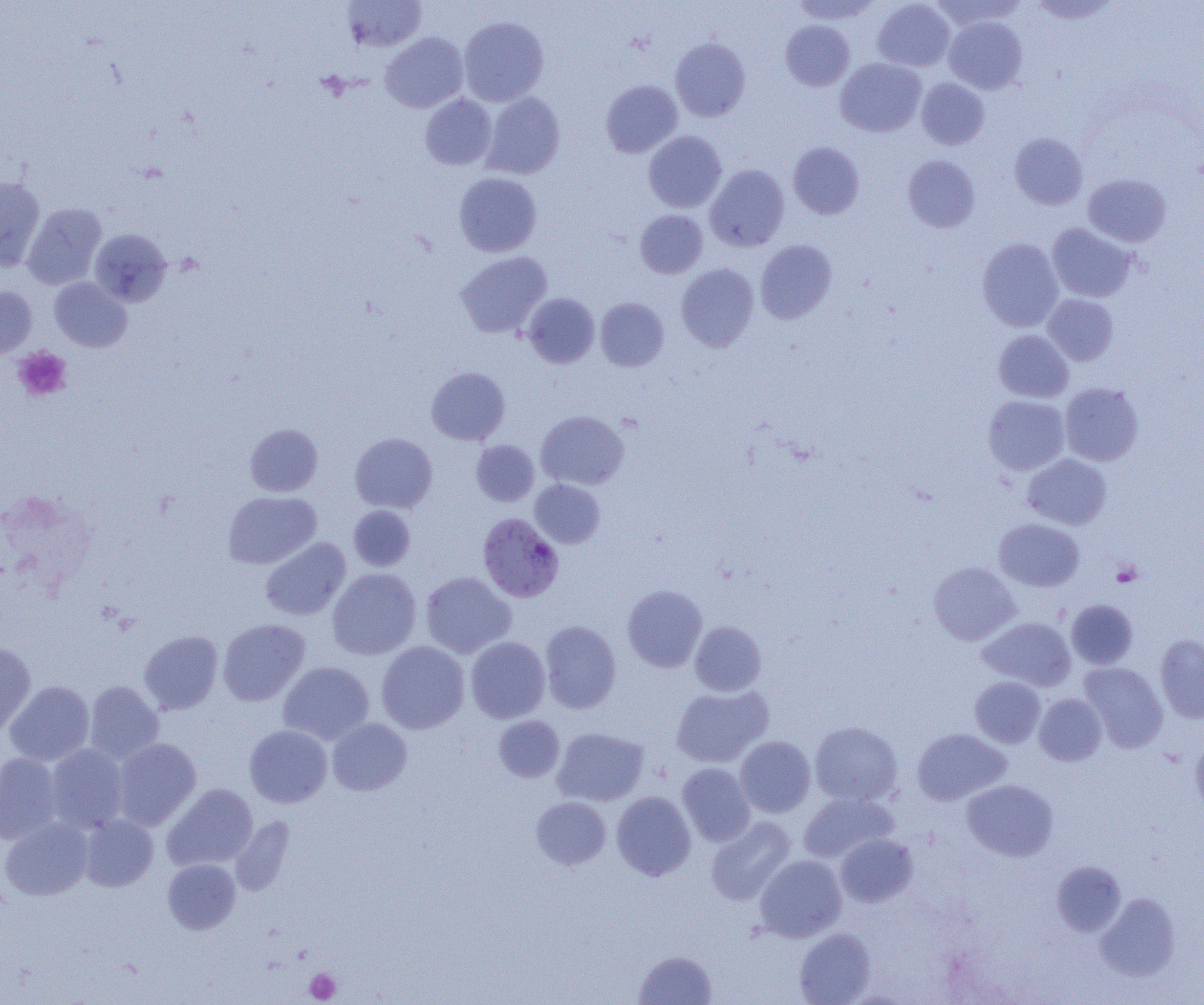
Summary:
  - Coordinate format: approximate bounding boxes as named x1/y1/x2/y2 corners in pixels
  - Platelet locations: (x1=14, y1=347, x2=72, y2=401), (x1=1111, y1=561, x2=1143, y2=587), (x1=305, y1=968, x2=341, y2=1003)
  - Uninfected red blood cell locations: (x1=791, y1=0, x2=881, y2=26), (x1=872, y1=0, x2=955, y2=72), (x1=928, y1=0, x2=1027, y2=31), (x1=341, y1=1, x2=427, y2=51), (x1=458, y1=16, x2=549, y2=107), (x1=943, y1=16, x2=1027, y2=94), (x1=780, y1=20, x2=855, y2=90), (x1=380, y1=32, x2=469, y2=112), (x1=670, y1=37, x2=750, y2=121), (x1=835, y1=58, x2=926, y2=137), (x1=916, y1=78, x2=989, y2=150), (x1=600, y1=80, x2=682, y2=158), (x1=481, y1=92, x2=565, y2=179), (x1=419, y1=94, x2=497, y2=170), (x1=643, y1=130, x2=726, y2=213), (x1=1009, y1=132, x2=1088, y2=210), (x1=788, y1=141, x2=865, y2=219), (x1=903, y1=155, x2=980, y2=232), (x1=705, y1=164, x2=789, y2=251), (x1=454, y1=172, x2=541, y2=257), (x1=1083, y1=174, x2=1171, y2=247), (x1=0, y1=176, x2=45, y2=270), (x1=22, y1=203, x2=106, y2=290), (x1=635, y1=210, x2=708, y2=279), (x1=1047, y1=223, x2=1137, y2=302), (x1=89, y1=229, x2=172, y2=307), (x1=977, y1=238, x2=1063, y2=332), (x1=755, y1=240, x2=837, y2=324), (x1=455, y1=251, x2=552, y2=338), (x1=676, y1=263, x2=759, y2=351), (x1=49, y1=277, x2=132, y2=352), (x1=0, y1=286, x2=37, y2=359), (x1=522, y1=293, x2=600, y2=368), (x1=1042, y1=294, x2=1118, y2=366), (x1=595, y1=297, x2=669, y2=371), (x1=993, y1=330, x2=1074, y2=403), (x1=427, y1=367, x2=510, y2=445), (x1=1060, y1=382, x2=1144, y2=466), (x1=983, y1=395, x2=1070, y2=475), (x1=535, y1=410, x2=629, y2=490), (x1=245, y1=423, x2=323, y2=497), (x1=350, y1=433, x2=438, y2=513), (x1=471, y1=440, x2=539, y2=506), (x1=1022, y1=454, x2=1112, y2=530), (x1=530, y1=479, x2=605, y2=548), (x1=223, y1=491, x2=321, y2=569), (x1=348, y1=505, x2=416, y2=571), (x1=994, y1=518, x2=1085, y2=591), (x1=260, y1=537, x2=351, y2=620), (x1=929, y1=562, x2=1021, y2=645), (x1=327, y1=568, x2=421, y2=660), (x1=420, y1=571, x2=516, y2=658), (x1=622, y1=584, x2=707, y2=672), (x1=1066, y1=599, x2=1138, y2=669), (x1=978, y1=616, x2=1076, y2=691), (x1=217, y1=619, x2=310, y2=706), (x1=540, y1=620, x2=621, y2=713), (x1=689, y1=621, x2=766, y2=695), (x1=139, y1=630, x2=223, y2=714), (x1=1155, y1=634, x2=1204, y2=723), (x1=466, y1=636, x2=550, y2=723), (x1=376, y1=641, x2=470, y2=734), (x1=0, y1=643, x2=36, y2=738), (x1=278, y1=661, x2=374, y2=745), (x1=1079, y1=662, x2=1168, y2=752), (x1=970, y1=676, x2=1046, y2=748), (x1=4, y1=680, x2=95, y2=766), (x1=84, y1=681, x2=163, y2=763), (x1=671, y1=685, x2=773, y2=768), (x1=1034, y1=694, x2=1107, y2=766), (x1=493, y1=715, x2=565, y2=783), (x1=328, y1=718, x2=412, y2=795), (x1=809, y1=721, x2=902, y2=806), (x1=244, y1=724, x2=332, y2=807), (x1=552, y1=727, x2=649, y2=806), (x1=912, y1=728, x2=1011, y2=805), (x1=735, y1=736, x2=816, y2=818), (x1=1190, y1=736, x2=1204, y2=817), (x1=112, y1=738, x2=201, y2=830), (x1=45, y1=744, x2=129, y2=833), (x1=0, y1=753, x2=62, y2=844), (x1=677, y1=762, x2=756, y2=846), (x1=962, y1=779, x2=1058, y2=861), (x1=163, y1=783, x2=258, y2=870), (x1=611, y1=791, x2=696, y2=880), (x1=798, y1=792, x2=898, y2=863), (x1=531, y1=797, x2=611, y2=870), (x1=78, y1=815, x2=158, y2=891), (x1=705, y1=816, x2=796, y2=905), (x1=0, y1=817, x2=94, y2=901), (x1=835, y1=833, x2=917, y2=907), (x1=755, y1=855, x2=847, y2=942), (x1=163, y1=859, x2=240, y2=934), (x1=1051, y1=860, x2=1126, y2=937), (x1=1095, y1=892, x2=1181, y2=982), (x1=794, y1=927, x2=876, y2=1005), (x1=634, y1=950, x2=717, y2=1005)
  - Plasmodium falciparum-infected red blood cell locations: (x1=477, y1=513, x2=564, y2=602)
  - Slide-level diagnosis: Plasmodium falciparum
  - Preparation: thin blood film
  - Field of view: single
  - Modality: light microscopy
  - Image size: 1204×1005 pixels
  - Magnification: 1000x